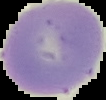

Summary:
  - Malaria status: uninfected
  - Preparation: thin blood film
  - Image size: 106×100 pixels
  - Image type: cell region segmented out of the field of view; surrounding area masked to black